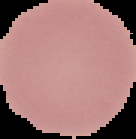
malaria status = uninfected
image size = 136×139 pixels
preparation = thin blood film
image type = segmented cell region with the area outside set to black